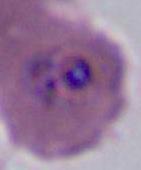
magnification = 400x or 1000x
modality = photomicrograph
identification = Plasmodium